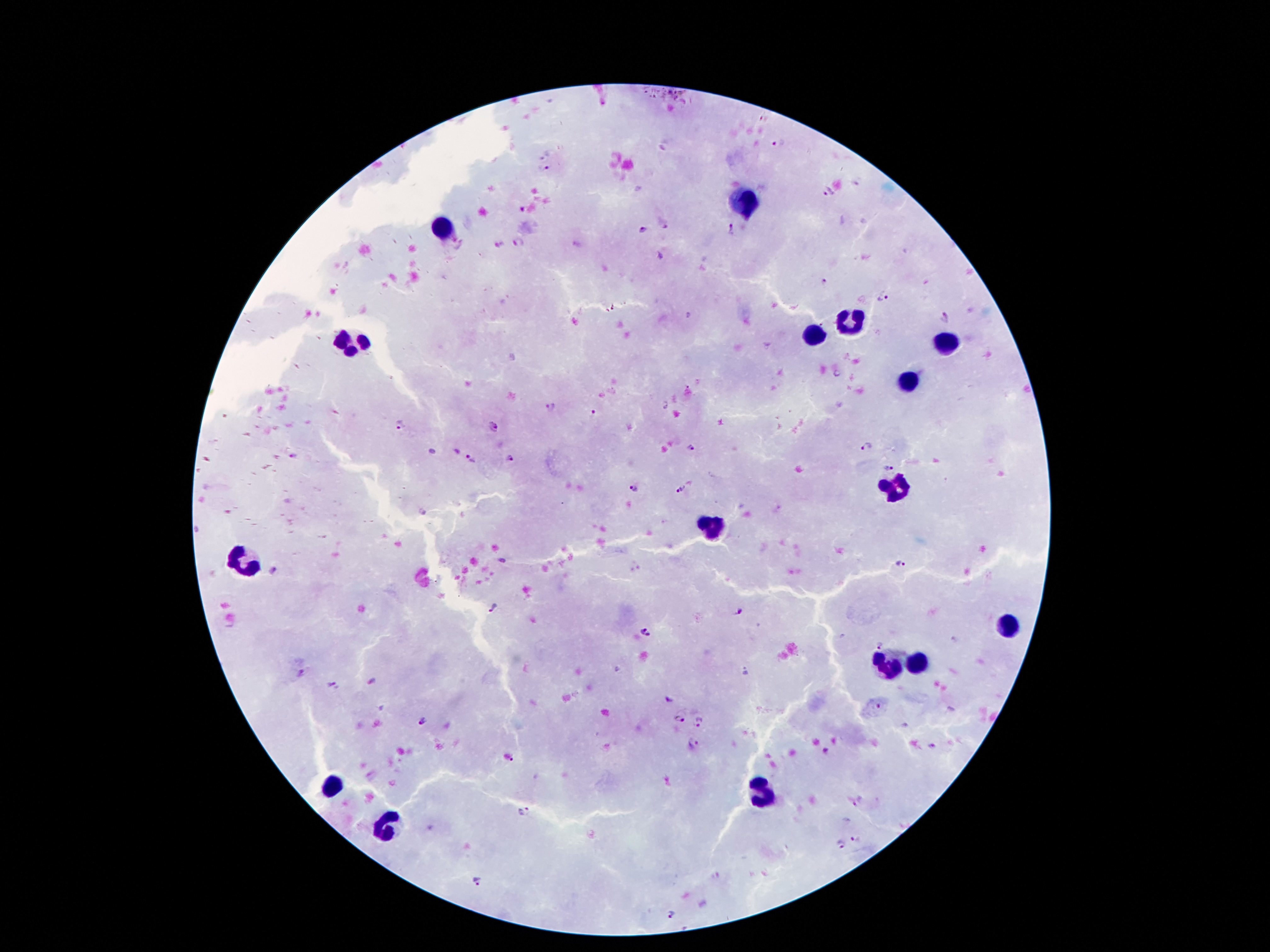

Approximate centers as {x, y} in pixels.
Summary:
  - Leukocyte locations: {746, 203}, {442, 229}, {851, 324}, {813, 337}, {350, 339}, {944, 345}, {910, 378}, {897, 488}, {711, 529}, {242, 561}, {1013, 626}, {914, 664}, {884, 665}, {335, 787}, {761, 790}, {391, 826}
  - Plasmodium parasite locations: {778, 142}, {546, 155}, {546, 170}, {827, 192}, {663, 224}, {730, 228}, {645, 231}, {522, 242}, {499, 246}, {824, 281}, {883, 299}, {945, 317}, {550, 408}, {593, 414}, {400, 426}, {494, 426}, {866, 446}, {689, 447}, {292, 456}, {509, 458}, {471, 460}, {890, 467}, {635, 489}, {679, 489}, {902, 564}, {272, 572}, {493, 608}, {741, 612}, {644, 634}, {879, 644}, {304, 674}, {332, 685}, {876, 706}, {678, 719}, {702, 722}, {423, 723}, {694, 745}, {826, 752}, {513, 761}, {525, 813}, {855, 839}, {839, 844}, {476, 881}, {675, 914}
  - Field of view: one from this slide
  - Patient malaria status: positive for Plasmodium falciparum
  - Image size: 1270×952 pixels
  - Preparation: thick peripheral-blood smear
  - Magnification: 100x
  - Stain: Giemsa
  - Capture: smartphone camera through the microscope eyepiece